Describe the morphology of the erythrocytes.
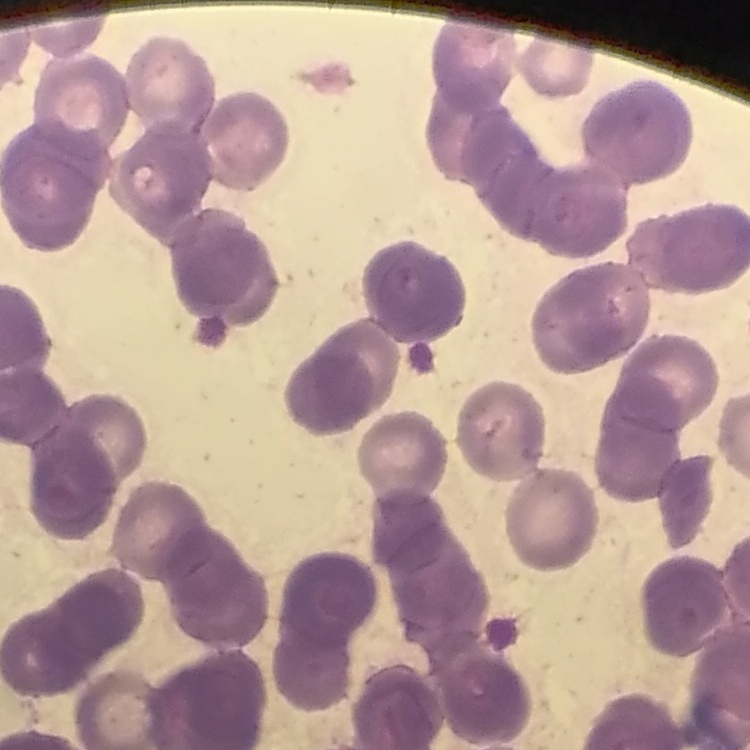
Rouleaux formation.

Square crop of a larger photomicrograph. Thin peripheral smear. Field's or Giemsa stain.